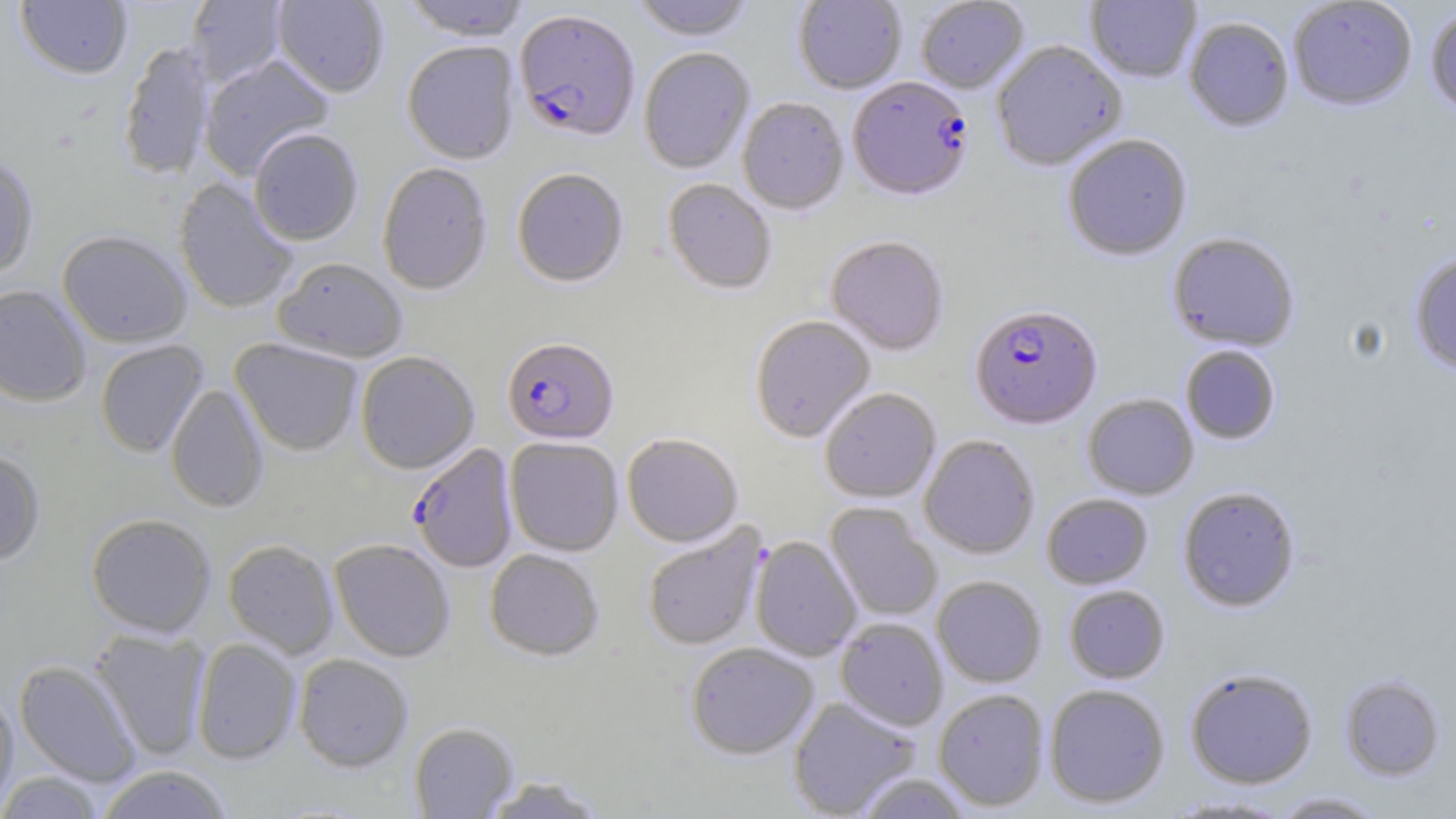
slide-level diagnosis = Plasmodium falciparum
modality = optical microscopy
image size = 1456×819 pixels
stain = May-Grünwald-Giemsa
field of view = one of a larger specimen
uninfected red blood cell locations = approximate bounding boxes as (x1,y1)-(x2,y2) corner pairs in pixels: (15,0)-(132,80), (184,0)-(288,87), (271,0)-(389,97), (401,0)-(531,42), (631,0)-(756,43), (793,0)-(906,95), (916,0)-(1028,94), (1085,0)-(1201,85), (1288,0)-(1417,111), (1425,5)-(1456,117), (1183,17)-(1294,133), (118,41)-(216,181), (402,42)-(520,164), (991,42)-(1127,172), (639,49)-(754,175), (198,55)-(335,180), (737,98)-(849,217), (248,129)-(363,246), (1063,135)-(1192,262), (0,152)-(39,281), (377,163)-(492,296), (512,169)-(629,289), (173,178)-(298,315), (662,180)-(776,296), (57,229)-(192,347), (1166,234)-(1300,352), (826,237)-(948,357), (1408,251)-(1456,375), (272,258)-(408,363), (0,285)-(92,406), (750,316)-(875,443), (230,337)-(363,456), (94,340)-(209,458), (1180,345)-(1281,445), (355,351)-(479,474), (165,384)-(269,513), (819,388)-(941,503), (1083,394)-(1198,500), (622,433)-(742,548), (919,435)-(1039,559), (505,437)-(623,557), (0,449)-(45,566), (1177,486)-(1300,613), (1041,494)-(1153,589), (825,503)-(942,621), (85,513)-(216,637), (641,524)-(767,651), (750,536)-(861,661), (222,539)-(339,658), (329,539)-(455,662), (484,548)-(604,661), (932,576)-(1046,687), (1063,585)-(1170,684), (835,618)-(948,730), (89,629)-(211,761), (192,638)-(301,764), (686,642)-(818,759), (293,653)-(413,772), (14,659)-(141,787), (1185,667)-(1318,788), (1339,674)-(1445,780), (1044,683)-(1170,808), (0,687)-(18,816), (933,688)-(1049,810), (788,696)-(920,817), (408,722)-(518,818), (97,765)-(233,819), (0,771)-(107,818), (852,772)-(975,818), (479,775)-(609,818), (1270,791)-(1389,818), (1162,795)-(1295,817)
magnification = 1000x
preparation = thin blood smear
Plasmodium falciparum-infected red blood cell locations = approximate bounding boxes as (x1,y1)-(x2,y2) corner pairs in pixels: (514,12)-(640,144), (848,79)-(974,203), (970,305)-(1102,430), (502,337)-(619,446), (408,443)-(519,572)